Locate every leukocyte (white blood cell).
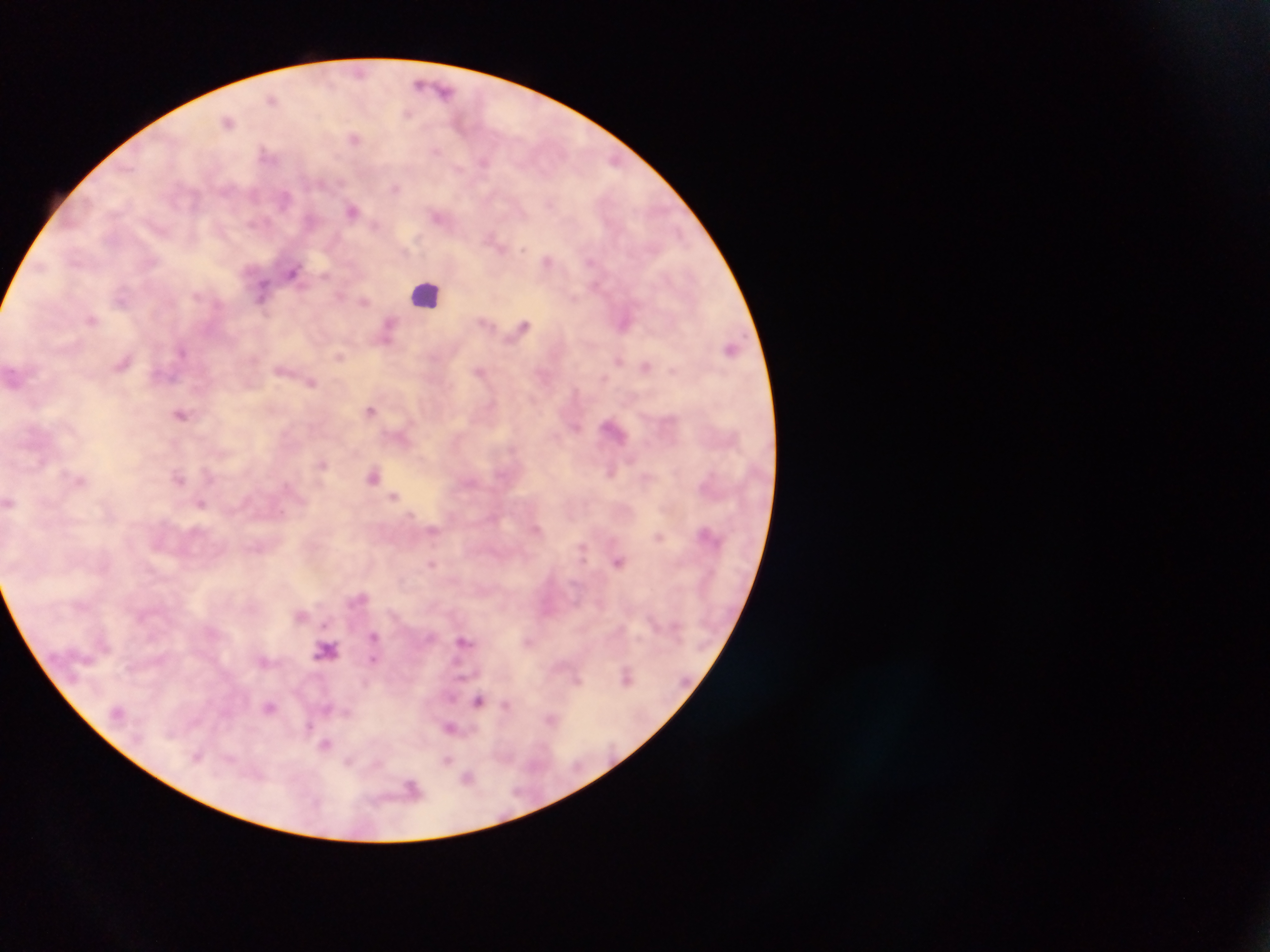
Approximate centers as (x, y) in pixels.
Leukocytes: (427, 294), (326, 650).

Plasmodium parasite locations: (359, 72), (420, 83), (445, 90), (272, 98), (407, 114), (228, 121), (354, 138), (436, 151), (265, 152), (613, 159), (484, 161), (459, 168), (396, 188), (284, 198), (549, 203), (352, 210), (437, 216), (374, 225), (493, 240), (523, 249), (547, 260), (590, 262), (41, 268), (293, 271), (324, 275), (595, 285), (263, 289), (340, 295), (574, 298), (364, 301), (91, 319), (626, 323), (524, 325), (389, 326), (387, 341), (731, 348), (182, 351), (340, 356), (619, 361), (123, 363), (645, 367), (479, 371), (311, 383), (371, 410), (181, 415), (576, 427), (323, 464), (610, 472), (373, 476), (179, 478), (394, 496), (201, 504), (433, 530), (706, 533), (659, 537), (618, 562), (431, 564), (301, 615), (325, 624), (374, 636), (463, 640), (373, 659), (626, 677), (577, 681), (478, 702), (506, 705), (269, 707), (326, 708), (346, 712), (551, 718), (307, 727), (449, 728), (326, 745), (447, 759), (348, 763), (468, 777), (412, 788). Image is 1270×952 pixels. Thick blood film. Single field of view. Collected in Ghana. Photographed through a microscope with a mobile-phone camera.